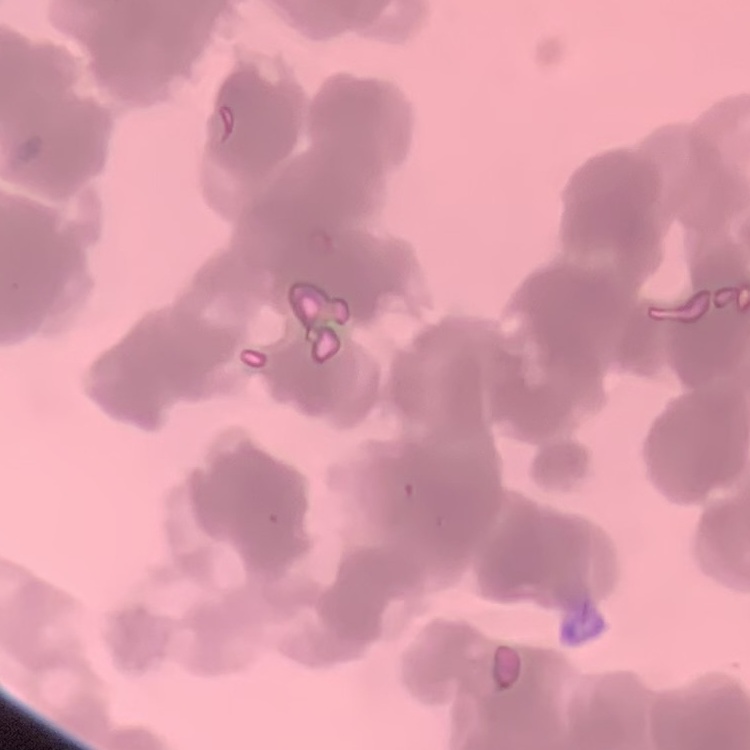

Summary:
  - Erythrocyte morphology: rouleaux formation
  - Image type: one tile cut from a larger photomicrograph
  - Stain: Field's or Giemsa
  - Preparation: thin peripheral smear